Assess this cell for malaria.
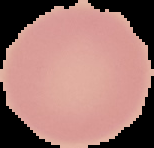
Uninfected.

From a thin blood smear. Image is 154×148 pixels. The area outside the segmented cell region is set to black.